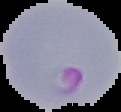

Malaria status: parasitized. Cell region segmented out of the field of view; the surrounding area is masked to black. Image is 121×112 pixels. From a thin blood smear.